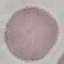 Result: no malaria parasites detected. Thin blood film. Acquired by smartphone through the microscope eyepiece. Giemsa-stained preparation. Automatically extracted cell patch, resized to 64 × 64 pixels.